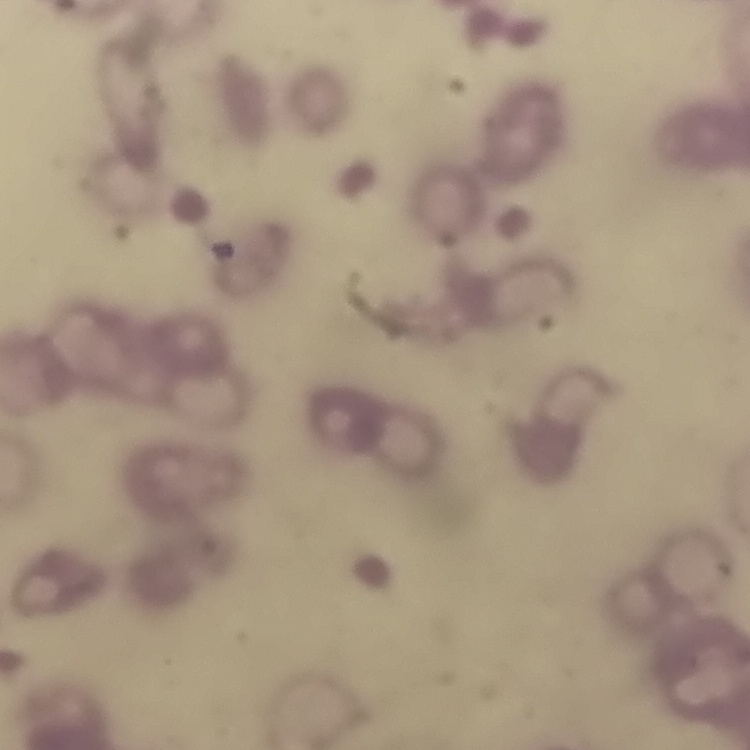 The erythrocytes show rouleaux formation. Stained with either Field's or Giemsa. Thin peripheral smear. One tile cut from a larger photomicrograph.